Give the extent of all Plasmodium vivax-infected red blood cells.
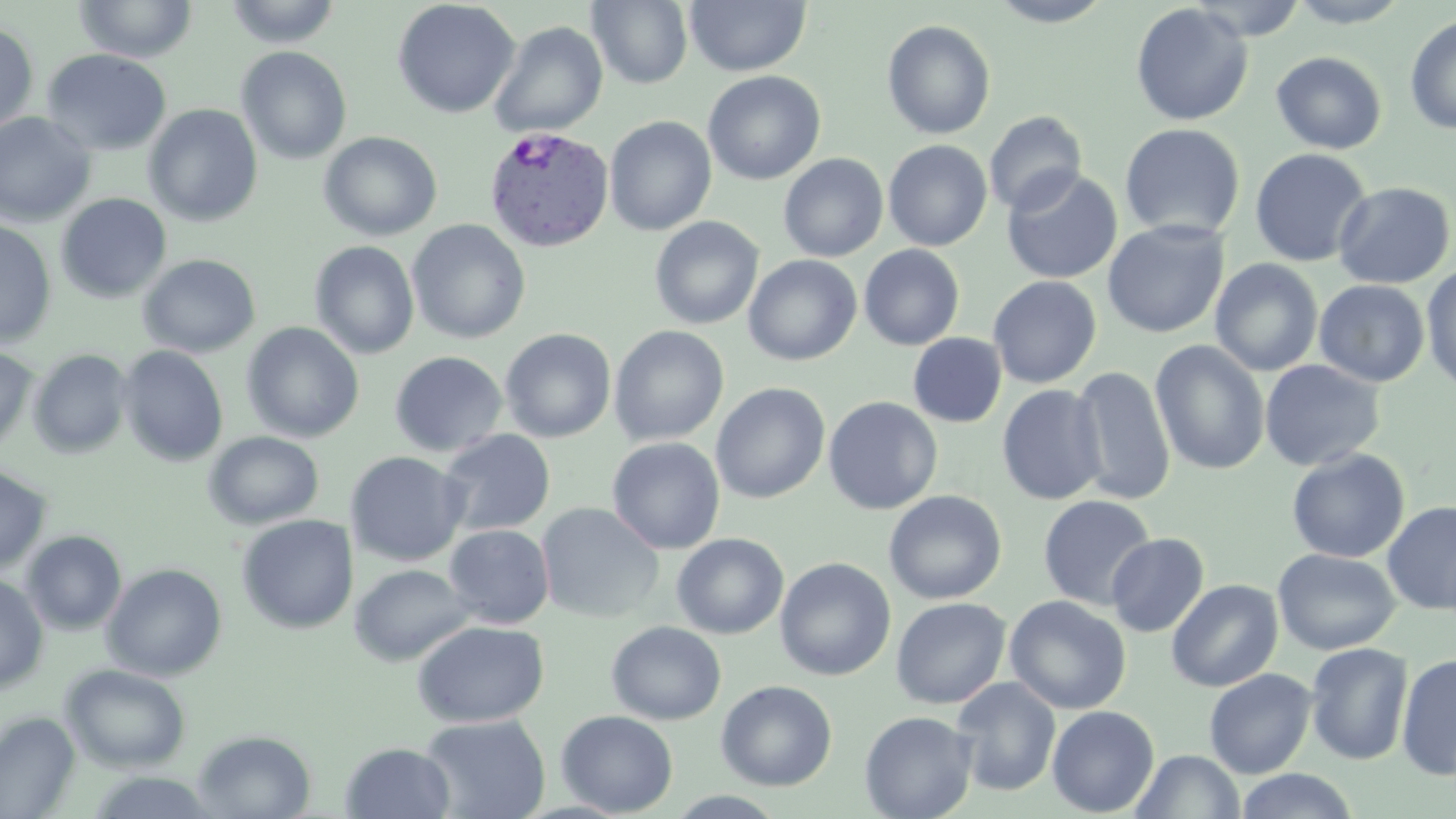

Approximate bounding boxes as [x1, y1, x2, y2] in pixels.
Plasmodium vivax-infected red blood cells: [484, 127, 614, 252].

slide-level diagnosis = Plasmodium vivax
field of view = single
uninfected red blood cell locations = approximate bounding boxes as [x1, y1, x2, y2] in pixels: [73, 0, 198, 63], [223, 0, 343, 48], [392, 0, 520, 119], [587, 0, 693, 89], [685, 0, 810, 76], [985, 0, 1118, 27], [1283, 0, 1413, 27], [1130, 3, 1253, 126], [1404, 12, 1456, 135], [881, 20, 996, 140], [0, 21, 39, 136], [489, 21, 609, 138], [236, 46, 352, 165], [41, 48, 172, 156], [1270, 51, 1387, 154], [703, 70, 826, 185], [143, 104, 263, 227], [0, 111, 97, 227], [983, 111, 1088, 216], [604, 115, 716, 236], [1120, 123, 1245, 241], [318, 130, 443, 242], [883, 139, 992, 251], [1249, 148, 1372, 267], [778, 153, 889, 261], [1001, 168, 1123, 285], [1332, 181, 1455, 289], [55, 192, 172, 304], [649, 216, 764, 330], [407, 219, 530, 344], [1102, 219, 1229, 339], [0, 220, 57, 347], [309, 242, 419, 359], [859, 244, 965, 350], [137, 253, 261, 358], [743, 254, 862, 366], [1210, 259, 1323, 376], [1421, 265, 1456, 393], [988, 275, 1102, 389], [1314, 279, 1430, 387], [241, 322, 364, 443], [609, 325, 729, 446], [499, 328, 617, 443], [908, 333, 1006, 427], [1150, 340, 1270, 475], [0, 344, 38, 455], [118, 345, 229, 467], [28, 349, 133, 459], [389, 351, 508, 457], [1259, 359, 1386, 471], [1071, 365, 1175, 504], [710, 382, 830, 504], [997, 384, 1107, 505], [823, 396, 943, 515], [438, 429, 556, 537], [203, 431, 325, 530], [607, 437, 726, 554], [1286, 448, 1410, 563], [345, 451, 469, 566], [0, 464, 52, 576], [883, 489, 1007, 605], [1038, 494, 1157, 611], [1382, 500, 1456, 615], [536, 502, 664, 624], [236, 514, 358, 634], [444, 524, 555, 629], [21, 530, 127, 636], [671, 533, 789, 639], [1106, 533, 1209, 637], [1272, 548, 1401, 655], [774, 556, 896, 681], [101, 562, 227, 681], [349, 563, 476, 667], [0, 572, 49, 694], [1166, 579, 1283, 692], [1004, 595, 1131, 715], [890, 597, 1011, 709], [411, 620, 550, 727], [606, 621, 726, 725], [1305, 642, 1414, 765], [1396, 653, 1456, 782], [60, 664, 191, 774], [1204, 668, 1317, 779], [951, 677, 1061, 796], [716, 680, 838, 791], [1047, 705, 1159, 817], [555, 710, 678, 817], [859, 710, 977, 819], [1, 711, 81, 818], [419, 714, 550, 819], [193, 729, 316, 818], [340, 742, 455, 818], [1130, 749, 1245, 818], [1233, 769, 1361, 819], [84, 770, 222, 817]
preparation = thin blood film
stain = May-Grünwald-Giemsa
image size = 1456×819 pixels
magnification = 1000x
modality = optical microscopy